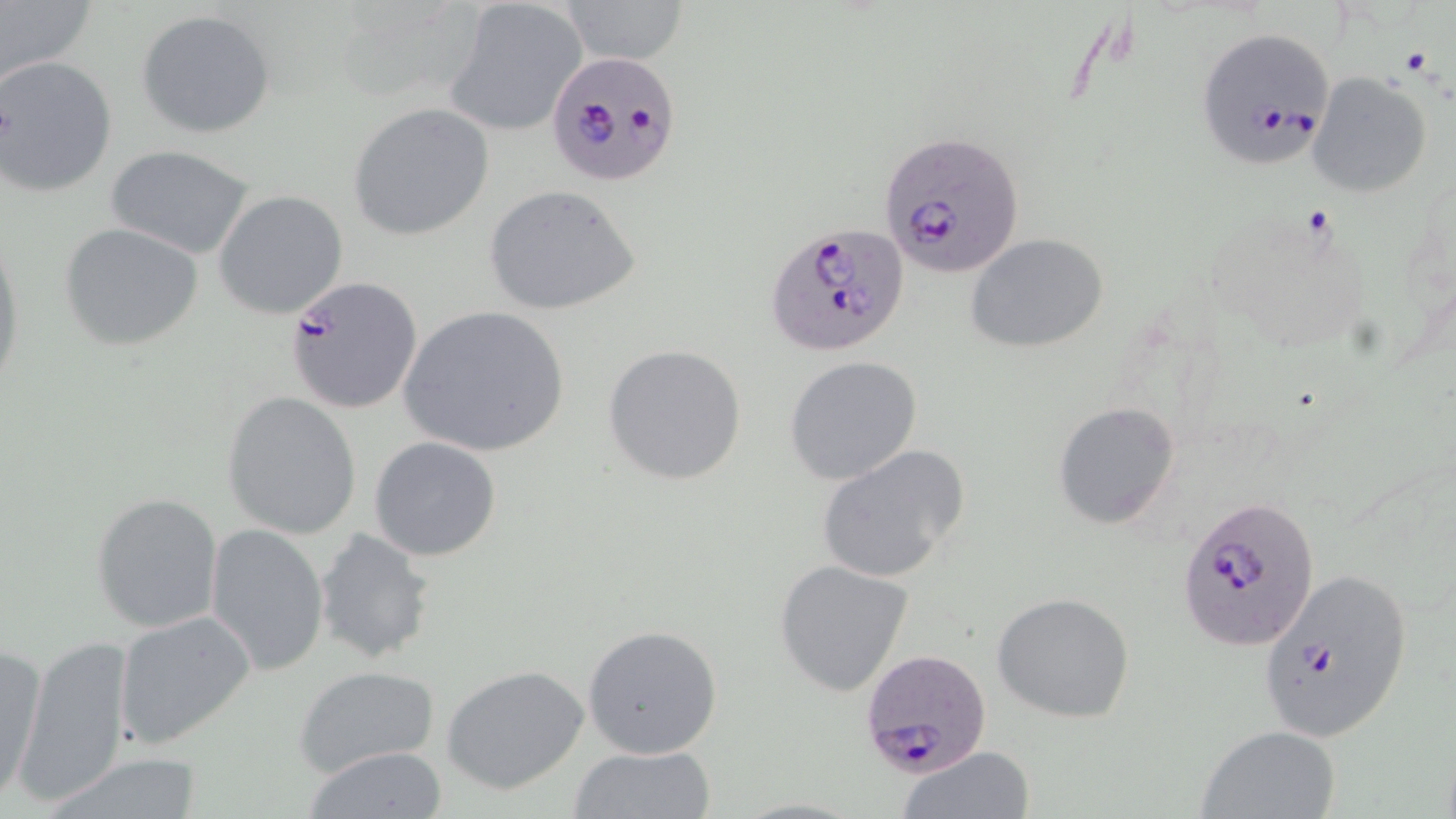

slide-level diagnosis = Plasmodium falciparum
preparation = thin blood film
field of view = one of a larger specimen
modality = optical microscopy
image size = 1456×819 pixels
magnification = 1000x
platelet locations = approximate bounding boxes as (x1, y1, x2, y2) in pixels: (1398, 45, 1433, 77)
uninfected red blood cell locations = approximate bounding boxes as (x1, y1, x2, y2) in pixels: (0, 0, 97, 89), (566, 0, 688, 66), (443, 1, 588, 134), (137, 9, 276, 139), (1, 56, 116, 195), (1306, 73, 1431, 199), (348, 102, 493, 239), (106, 145, 260, 260), (482, 185, 642, 315), (213, 189, 348, 319), (59, 223, 205, 352), (0, 227, 25, 399), (967, 235, 1109, 353), (398, 304, 571, 458), (602, 343, 747, 487), (786, 355, 923, 484), (222, 391, 364, 539), (1052, 401, 1181, 530), (369, 437, 502, 561), (818, 444, 970, 583), (90, 491, 223, 633), (205, 523, 329, 675), (314, 528, 436, 664), (772, 558, 917, 698), (991, 592, 1136, 723), (113, 610, 256, 751), (583, 625, 724, 761), (16, 635, 134, 805), (0, 644, 46, 807), (292, 664, 442, 778), (443, 665, 590, 796), (1195, 726, 1340, 819), (570, 744, 716, 819), (898, 745, 1036, 819), (302, 746, 449, 818), (40, 751, 209, 819)
Plasmodium falciparum-infected red blood cell locations = approximate bounding boxes as (x1, y1, x2, y2) in pixels: (1204, 33, 1335, 174), (548, 54, 679, 187), (879, 132, 1023, 276), (765, 222, 912, 359), (285, 275, 422, 414), (1179, 497, 1320, 648), (1255, 567, 1415, 746), (862, 647, 992, 777)
stain = May-Grünwald-Giemsa